Outline platelets.
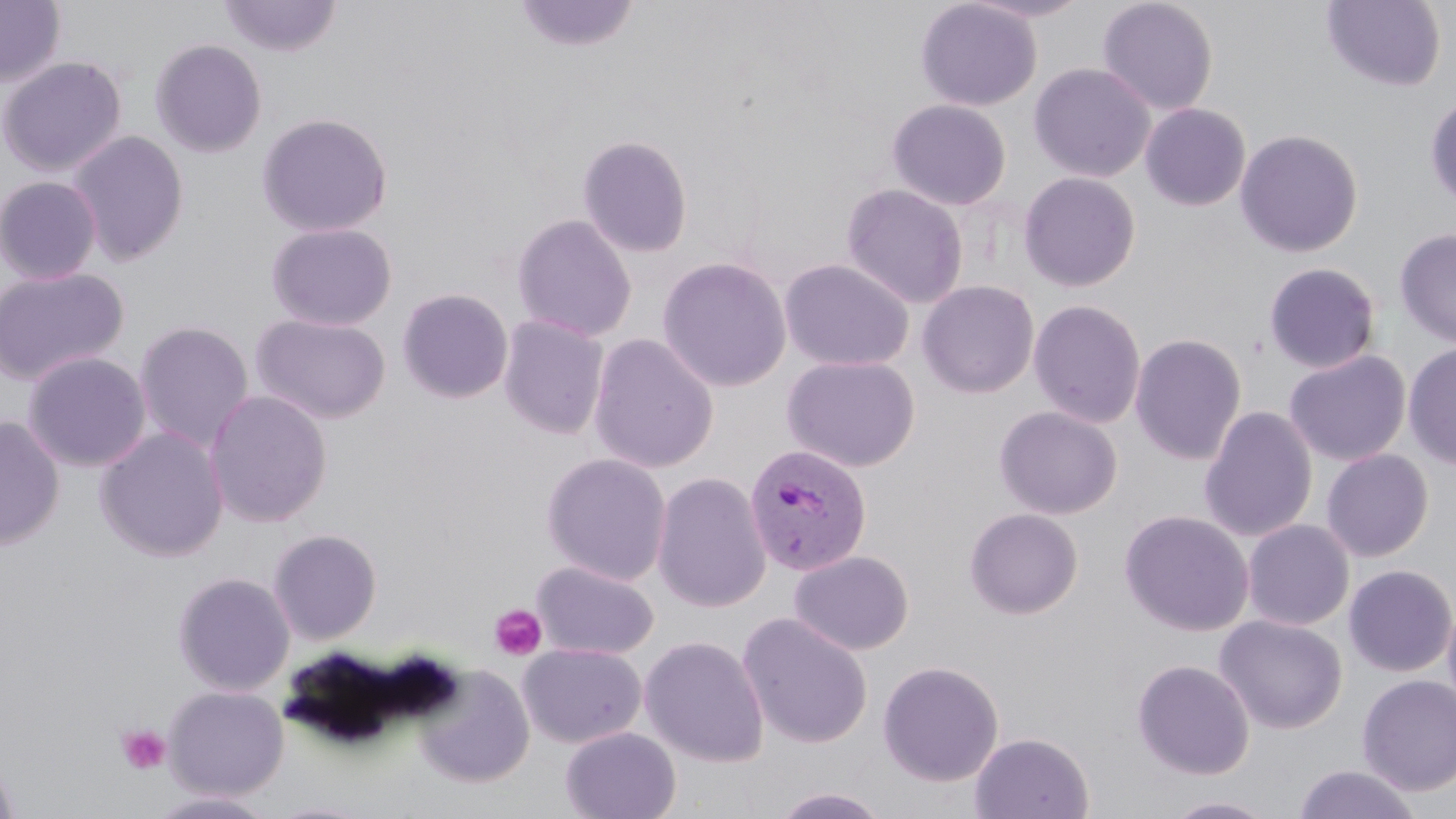
Approximate bounding boxes as (x1, y1, x2, y2) in pixels.
Platelets: (488, 603, 548, 661), (116, 724, 172, 775).

Uninfected red blood cell locations: (0, 0, 66, 88), (219, 0, 343, 58), (512, 0, 640, 54), (915, 0, 1042, 111), (961, 0, 1094, 23), (1097, 0, 1219, 116), (1322, 1, 1446, 91), (149, 38, 268, 158), (0, 56, 126, 177), (1028, 62, 1155, 182), (1425, 94, 1456, 210), (887, 99, 1011, 210), (1140, 103, 1251, 211), (256, 112, 393, 237), (1235, 129, 1363, 257), (67, 130, 190, 266), (577, 134, 693, 258), (1018, 172, 1140, 292), (0, 176, 103, 285), (840, 183, 968, 309), (512, 213, 637, 342), (265, 221, 397, 331), (1394, 227, 1456, 349), (657, 256, 792, 392), (779, 258, 914, 372), (1263, 262, 1381, 374), (0, 266, 129, 386), (917, 280, 1040, 399), (397, 287, 514, 404), (1028, 299, 1146, 428), (252, 313, 391, 424), (497, 314, 609, 439), (134, 319, 254, 453), (1130, 332, 1247, 465), (587, 333, 720, 473), (1403, 342, 1456, 471), (1285, 349, 1411, 466), (22, 351, 152, 472), (782, 355, 921, 472), (204, 389, 333, 528), (994, 405, 1122, 519), (1199, 405, 1319, 542), (0, 414, 65, 550), (95, 426, 229, 562), (1321, 449, 1434, 562), (541, 452, 672, 585), (652, 472, 772, 613), (964, 507, 1084, 619), (1119, 509, 1254, 636), (1242, 519, 1355, 631), (268, 528, 382, 645), (789, 550, 914, 656), (531, 560, 659, 660), (1343, 564, 1456, 677), (172, 571, 295, 696), (1442, 597, 1456, 716), (737, 613, 873, 748), (1215, 615, 1348, 734), (639, 635, 770, 766), (518, 643, 646, 748), (1132, 659, 1254, 780), (877, 660, 1004, 786), (415, 665, 535, 787), (1357, 675, 1456, 796), (164, 685, 289, 800), (561, 727, 681, 819), (970, 732, 1094, 818), (0, 750, 20, 819), (1292, 764, 1423, 819), (770, 787, 891, 818), (146, 790, 279, 818), (1161, 796, 1278, 818). Plasmodium vivax-infected red blood cell locations: (744, 443, 873, 577). Slide-level diagnosis: Plasmodium vivax. Single field of view. Optical microscopy. 1000x magnification. Image is 1456×819 pixels. Thin blood film. May-Grünwald-Giemsa-stained preparation.